Locate every Plasmodium falciparum-infected red blood cell.
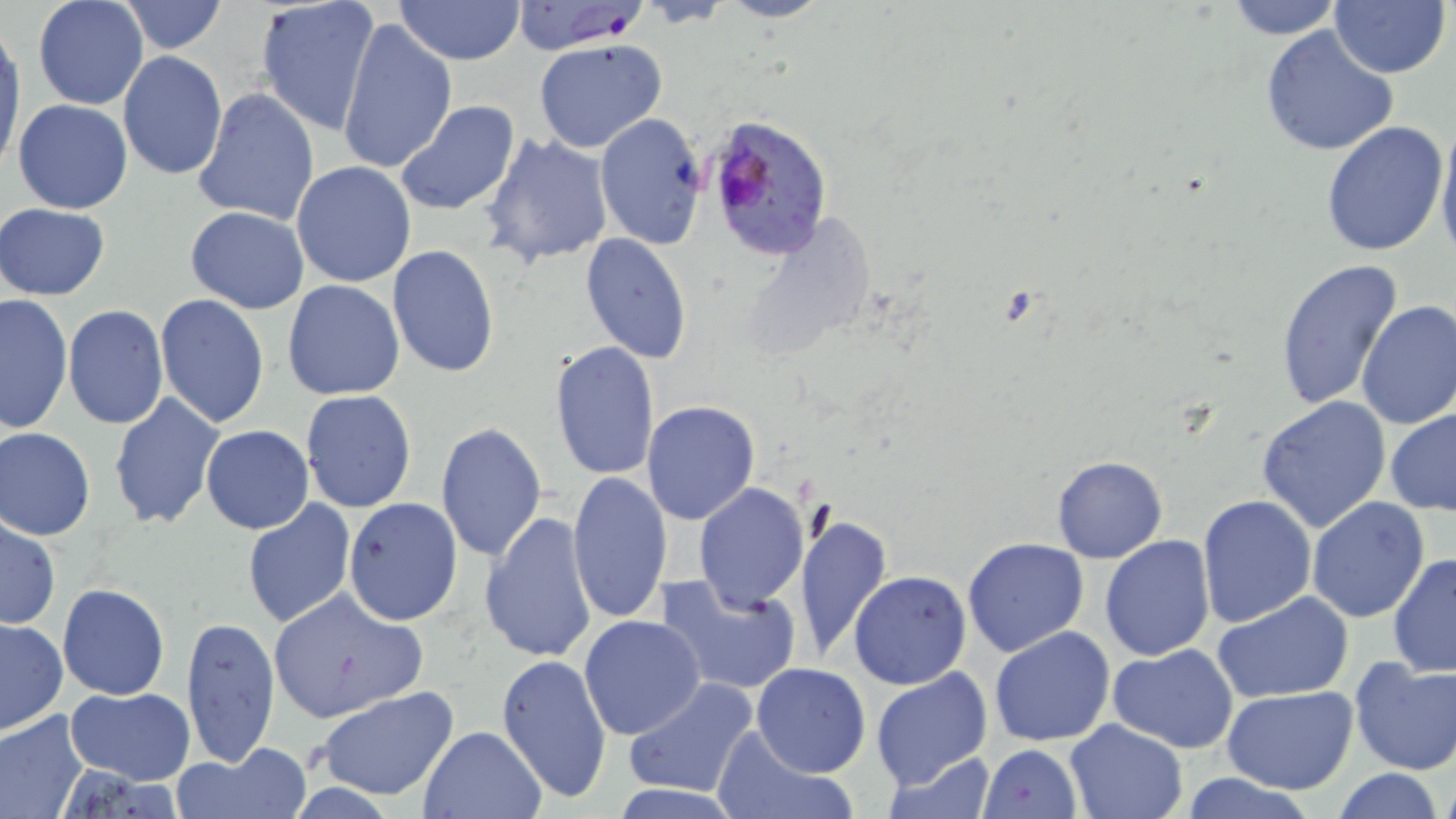
Approximate bounding boxes as [x1, y1, x2, y2] in pixels.
Plasmodium falciparum-infected red blood cells: [509, 2, 649, 54], [706, 110, 835, 261].

slide_level_diagnosis: Plasmodium falciparum
uninfected_red_blood_cell_locations: 'approximate bounding boxes as [x1, y1, x2, y2] in pixels: [254, 0, 379, 136], [393, 0, 525, 65], [717, 0, 829, 23], [1221, 0, 1348, 39], [33, 1, 150, 110], [117, 1, 228, 54], [1329, 2, 1450, 79], [337, 19, 458, 175], [1, 25, 24, 168], [1260, 25, 1401, 157], [534, 38, 667, 154], [118, 51, 228, 179], [191, 89, 320, 225], [12, 99, 132, 215], [394, 100, 522, 217], [593, 111, 709, 251], [1433, 117, 1456, 261], [1319, 120, 1449, 257], [481, 132, 615, 269], [292, 161, 417, 287], [1, 202, 109, 300], [186, 206, 309, 313], [580, 233, 693, 364], [387, 245, 498, 377], [1274, 259, 1404, 413], [283, 279, 405, 400], [0, 293, 74, 433], [155, 294, 270, 428], [1355, 299, 1456, 430], [64, 305, 168, 430], [549, 340, 660, 481], [300, 390, 417, 512], [108, 393, 225, 530], [1256, 396, 1392, 533], [642, 401, 760, 524], [1384, 407, 1456, 517], [434, 422, 548, 562], [201, 424, 315, 534], [0, 427, 96, 540], [1051, 456, 1168, 564], [566, 471, 674, 624], [694, 483, 809, 612], [1196, 495, 1319, 629], [1306, 497, 1432, 622], [242, 498, 357, 631], [343, 498, 463, 626], [479, 511, 597, 664], [794, 514, 892, 661], [1, 517, 61, 632], [1100, 536, 1215, 660], [962, 537, 1090, 657], [1388, 552, 1456, 679], [848, 570, 971, 689], [654, 572, 802, 696], [58, 583, 169, 700], [265, 587, 428, 724], [1212, 592, 1356, 705], [182, 614, 280, 766], [579, 616, 707, 741], [0, 619, 68, 735], [988, 626, 1116, 747], [1108, 644, 1240, 751], [496, 653, 612, 802], [1350, 655, 1455, 775], [751, 663, 871, 778], [870, 667, 994, 791], [626, 679, 759, 800], [67, 686, 195, 784], [1221, 686, 1359, 794], [316, 687, 459, 799], [0, 708, 91, 819], [1063, 718, 1188, 819], [418, 724, 548, 818], [711, 726, 853, 819], [978, 744, 1083, 819], [175, 746, 311, 819], [879, 750, 999, 818], [1329, 768, 1447, 819], [1176, 775, 1321, 819], [607, 784, 747, 818]'
stain: May-Grünwald-Giemsa
image_size: 1456×819 pixels
field_of_view: single
magnification: 1000x
modality: optical microscopy
preparation: thin blood film